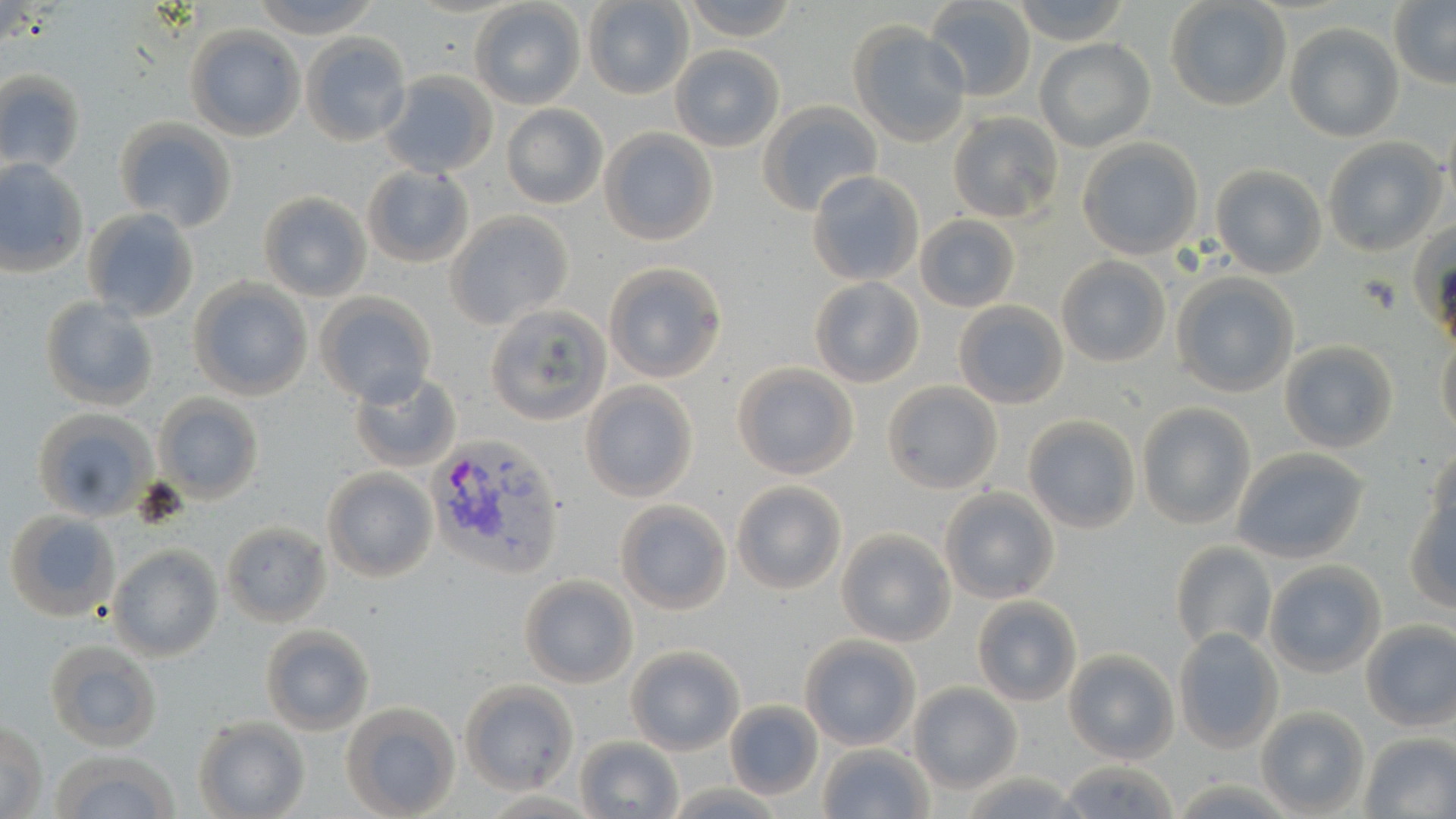

Summary:
  - Coordinate format: approximate bounding boxes as named x1/y1/x2/y2 corners in pixels
  - Uninfected red blood cell locations: (x1=246, y1=0, x2=385, y2=37), (x1=680, y1=0, x2=800, y2=42), (x1=1009, y1=0, x2=1130, y2=46), (x1=1164, y1=0, x2=1292, y2=112), (x1=583, y1=1, x2=694, y2=100), (x1=468, y1=2, x2=587, y2=110), (x1=924, y1=2, x2=1037, y2=101), (x1=1388, y1=3, x2=1456, y2=86), (x1=848, y1=22, x2=970, y2=147), (x1=1283, y1=22, x2=1404, y2=142), (x1=185, y1=25, x2=306, y2=142), (x1=300, y1=33, x2=410, y2=145), (x1=1035, y1=39, x2=1155, y2=152), (x1=669, y1=45, x2=785, y2=152), (x1=0, y1=70, x2=86, y2=175), (x1=378, y1=70, x2=498, y2=178), (x1=759, y1=102, x2=882, y2=215), (x1=501, y1=104, x2=609, y2=209), (x1=948, y1=111, x2=1063, y2=223), (x1=112, y1=119, x2=238, y2=233), (x1=598, y1=128, x2=718, y2=246), (x1=1077, y1=138, x2=1204, y2=259), (x1=1322, y1=138, x2=1446, y2=257), (x1=0, y1=158, x2=89, y2=276), (x1=361, y1=163, x2=475, y2=268), (x1=1210, y1=165, x2=1326, y2=278), (x1=808, y1=171, x2=926, y2=287), (x1=257, y1=192, x2=372, y2=303), (x1=82, y1=208, x2=198, y2=322), (x1=445, y1=211, x2=574, y2=330), (x1=915, y1=216, x2=1019, y2=310), (x1=1408, y1=222, x2=1456, y2=333), (x1=1057, y1=257, x2=1170, y2=367), (x1=602, y1=262, x2=727, y2=383), (x1=1170, y1=272, x2=1299, y2=397), (x1=809, y1=278, x2=923, y2=387), (x1=188, y1=279, x2=313, y2=400), (x1=315, y1=294, x2=436, y2=408), (x1=38, y1=296, x2=158, y2=413), (x1=953, y1=300, x2=1069, y2=408), (x1=484, y1=305, x2=611, y2=426), (x1=1437, y1=333, x2=1456, y2=442), (x1=1278, y1=340, x2=1398, y2=455), (x1=729, y1=362, x2=860, y2=480), (x1=347, y1=368, x2=461, y2=472), (x1=581, y1=381, x2=698, y2=502), (x1=881, y1=382, x2=1002, y2=494), (x1=153, y1=394, x2=264, y2=503), (x1=1136, y1=404, x2=1254, y2=530), (x1=32, y1=408, x2=157, y2=521), (x1=1022, y1=415, x2=1140, y2=534), (x1=1425, y1=446, x2=1455, y2=544), (x1=1230, y1=448, x2=1370, y2=565), (x1=322, y1=468, x2=436, y2=582), (x1=730, y1=481, x2=848, y2=596), (x1=940, y1=487, x2=1059, y2=603), (x1=1403, y1=496, x2=1456, y2=608), (x1=614, y1=500, x2=732, y2=614), (x1=5, y1=510, x2=119, y2=620), (x1=221, y1=522, x2=330, y2=626), (x1=837, y1=530, x2=955, y2=646), (x1=1170, y1=541, x2=1276, y2=653), (x1=108, y1=545, x2=224, y2=663), (x1=1262, y1=560, x2=1385, y2=677), (x1=519, y1=575, x2=637, y2=688), (x1=972, y1=596, x2=1081, y2=706), (x1=1359, y1=620, x2=1456, y2=730), (x1=259, y1=625, x2=374, y2=735), (x1=1172, y1=629, x2=1284, y2=752), (x1=799, y1=635, x2=923, y2=750), (x1=44, y1=638, x2=162, y2=751), (x1=625, y1=646, x2=744, y2=754), (x1=1064, y1=650, x2=1177, y2=764), (x1=459, y1=680, x2=578, y2=793), (x1=910, y1=684, x2=1021, y2=791), (x1=339, y1=701, x2=461, y2=819), (x1=727, y1=701, x2=823, y2=799), (x1=1257, y1=706, x2=1370, y2=817), (x1=1, y1=716, x2=48, y2=819), (x1=192, y1=716, x2=310, y2=819), (x1=1360, y1=733, x2=1456, y2=817), (x1=576, y1=735, x2=683, y2=818), (x1=816, y1=743, x2=934, y2=819), (x1=45, y1=748, x2=181, y2=819), (x1=1054, y1=759, x2=1179, y2=816), (x1=959, y1=770, x2=1085, y2=818)
  - Plasmodium vivax-infected red blood cell locations: (x1=424, y1=434, x2=566, y2=577)
  - Slide-level diagnosis: Plasmodium vivax
  - Modality: optical microscopy
  - Image size: 1456×819 pixels
  - Field of view: single
  - Preparation: thin blood smear
  - Magnification: 1000x
  - Stain: May-Grünwald-Giemsa